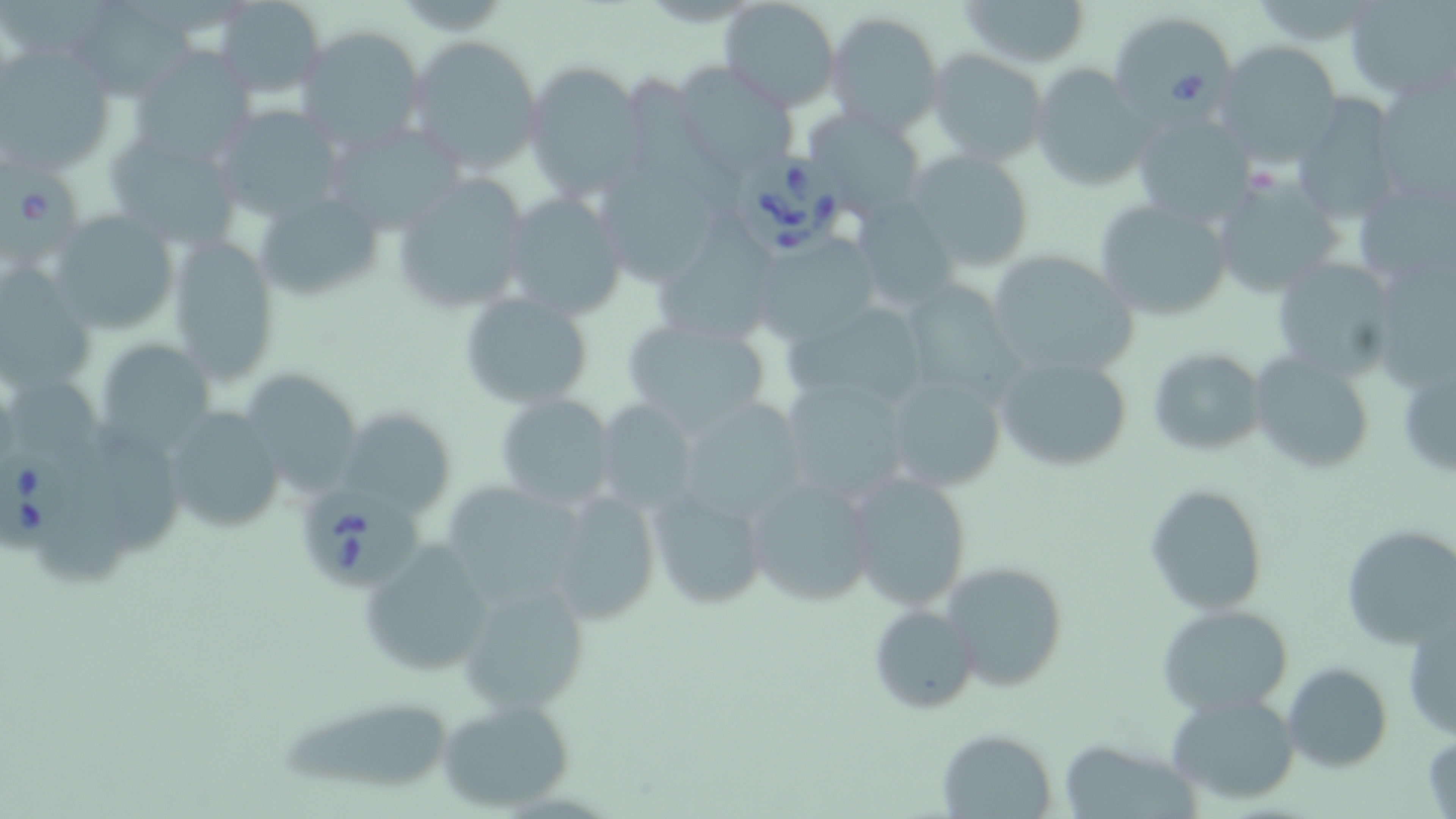
Approximate bounding boxes as (x1,y1)-(x2,y2) corner pairs in pixels. Babesia divergens-infected red blood cell locations: (1107,9)-(1236,119), (0,152)-(85,272), (734,152)-(846,264), (0,446)-(82,557), (299,481)-(428,590). Uninfected red blood cell locations: (956,0)-(1092,70), (1345,0)-(1456,98), (213,1)-(326,97), (719,1)-(840,113), (72,2)-(191,98), (824,13)-(942,135), (296,25)-(427,156), (405,33)-(545,175), (3,40)-(121,175), (1213,40)-(1344,163), (927,48)-(1049,165), (128,49)-(259,166), (524,61)-(650,201), (673,64)-(799,181), (1030,64)-(1154,191), (1374,73)-(1456,207), (1290,95)-(1404,227), (212,106)-(347,221), (804,108)-(929,220), (1130,112)-(1253,226), (324,124)-(463,235), (104,129)-(243,248), (905,151)-(1035,273), (1211,171)-(1344,297), (390,172)-(531,314), (1352,172)-(1456,292), (251,190)-(384,304), (499,190)-(627,320), (1093,197)-(1235,321), (49,210)-(181,334), (652,225)-(778,348), (168,233)-(282,384), (750,235)-(886,343), (985,249)-(1139,379), (1269,256)-(1401,381), (0,266)-(97,397), (893,277)-(1025,412), (458,290)-(594,412), (783,300)-(932,413), (621,315)-(772,433), (101,335)-(221,452), (1147,346)-(1269,456), (992,351)-(1136,474), (1251,352)-(1375,475), (1397,354)-(1456,485), (239,368)-(365,499), (882,373)-(1007,493), (778,375)-(915,507), (12,381)-(105,477), (494,392)-(616,511), (674,396)-(811,523), (593,399)-(699,514), (161,405)-(287,536), (338,408)-(456,516), (81,419)-(178,553), (843,468)-(975,611), (742,474)-(879,607), (42,476)-(134,588), (440,480)-(592,611), (1144,483)-(1269,616), (647,486)-(768,609), (547,489)-(662,628), (1341,523)-(1456,650), (359,541)-(493,678), (941,560)-(1068,693), (459,578)-(592,715), (867,603)-(980,714), (1157,604)-(1294,714), (1403,616)-(1455,743), (1282,662)-(1392,772), (1164,689)-(1300,806), (274,693)-(461,799), (434,699)-(574,811), (937,729)-(1057,817), (1423,729)-(1455,819). Slide-level diagnosis: Babesia divergens. Optical microscopy. Captured at 1000x magnification. Image is 1456×819 pixels. One field of a larger specimen. May-Grünwald-Giemsa stain. Thin blood film.